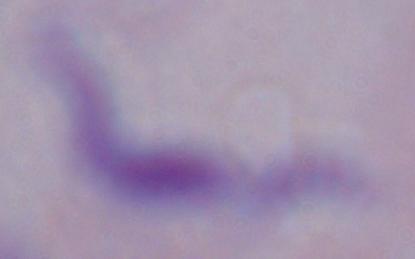
Summary:
  - Magnification: 1000x
  - Identification: trypanosome
  - Modality: photomicrograph